Locate every blood parasite and identify its species.
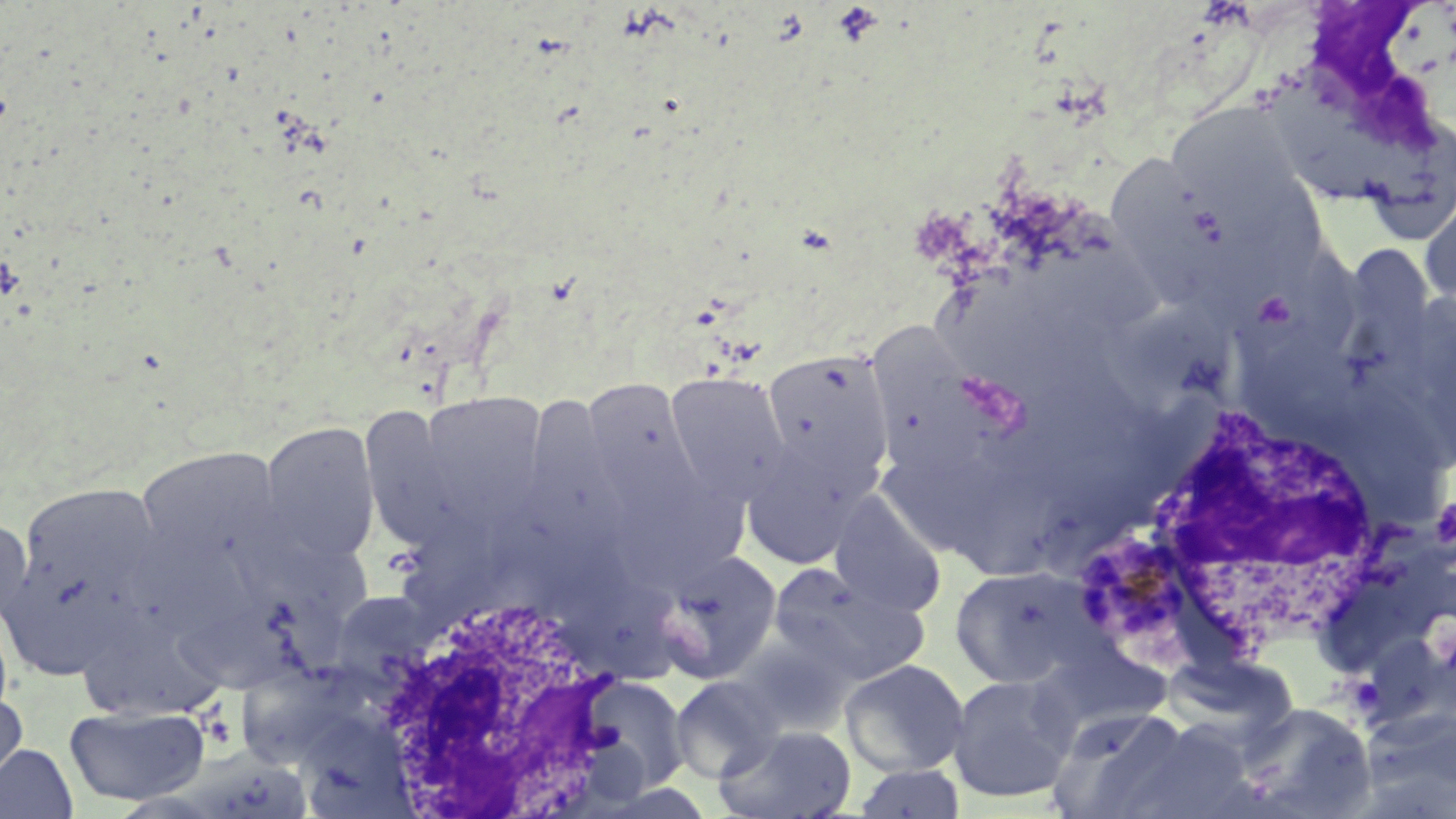
Approximate bounding boxes as named x1/y1/x2/y2 corners in pixels.
Plasmodium malariae-infected red blood cells: (x1=1072, y1=534, x2=1185, y2=645).
No Plasmodium falciparum, Plasmodium ovale, Plasmodium vivax, Babesia divergens, or Trypanosoma brucei observed.

Uninfected red blood cell locations: (x1=1270, y1=66, x2=1397, y2=206), (x1=1165, y1=103, x2=1309, y2=219), (x1=1359, y1=120, x2=1455, y2=253), (x1=1109, y1=155, x2=1224, y2=313), (x1=1419, y1=194, x2=1456, y2=315), (x1=1110, y1=301, x2=1249, y2=410), (x1=871, y1=324, x2=999, y2=478), (x1=761, y1=347, x2=895, y2=484), (x1=664, y1=371, x2=792, y2=505), (x1=581, y1=380, x2=707, y2=521), (x1=416, y1=391, x2=549, y2=527), (x1=358, y1=405, x2=470, y2=551), (x1=258, y1=420, x2=381, y2=567), (x1=739, y1=444, x2=869, y2=569), (x1=135, y1=445, x2=284, y2=576), (x1=606, y1=473, x2=748, y2=592), (x1=13, y1=479, x2=168, y2=647), (x1=829, y1=491, x2=946, y2=617), (x1=0, y1=516, x2=33, y2=628), (x1=650, y1=549, x2=783, y2=684), (x1=770, y1=563, x2=928, y2=682), (x1=949, y1=565, x2=1098, y2=688), (x1=176, y1=588, x2=346, y2=691), (x1=74, y1=627, x2=229, y2=722), (x1=1026, y1=650, x2=1173, y2=761), (x1=237, y1=658, x2=387, y2=773), (x1=840, y1=659, x2=970, y2=777), (x1=580, y1=674, x2=691, y2=794), (x1=947, y1=674, x2=1079, y2=804), (x1=670, y1=675, x2=784, y2=783), (x1=0, y1=692, x2=27, y2=785), (x1=1233, y1=702, x2=1376, y2=818), (x1=64, y1=705, x2=210, y2=806), (x1=1050, y1=706, x2=1190, y2=818), (x1=1123, y1=722, x2=1256, y2=819), (x1=715, y1=724, x2=856, y2=819), (x1=0, y1=743, x2=78, y2=819), (x1=852, y1=764, x2=967, y2=818). White blood cell locations: (x1=1147, y1=409, x2=1388, y2=648), (x1=345, y1=590, x2=630, y2=814). Platelet locations: (x1=1433, y1=495, x2=1456, y2=556). Slide-level diagnosis: Plasmodium malariae. 1000x magnification. Optical microscopy. Image is 1456×819 pixels. Single field of view. Thin blood smear. May-Grünwald-Giemsa-stained preparation.